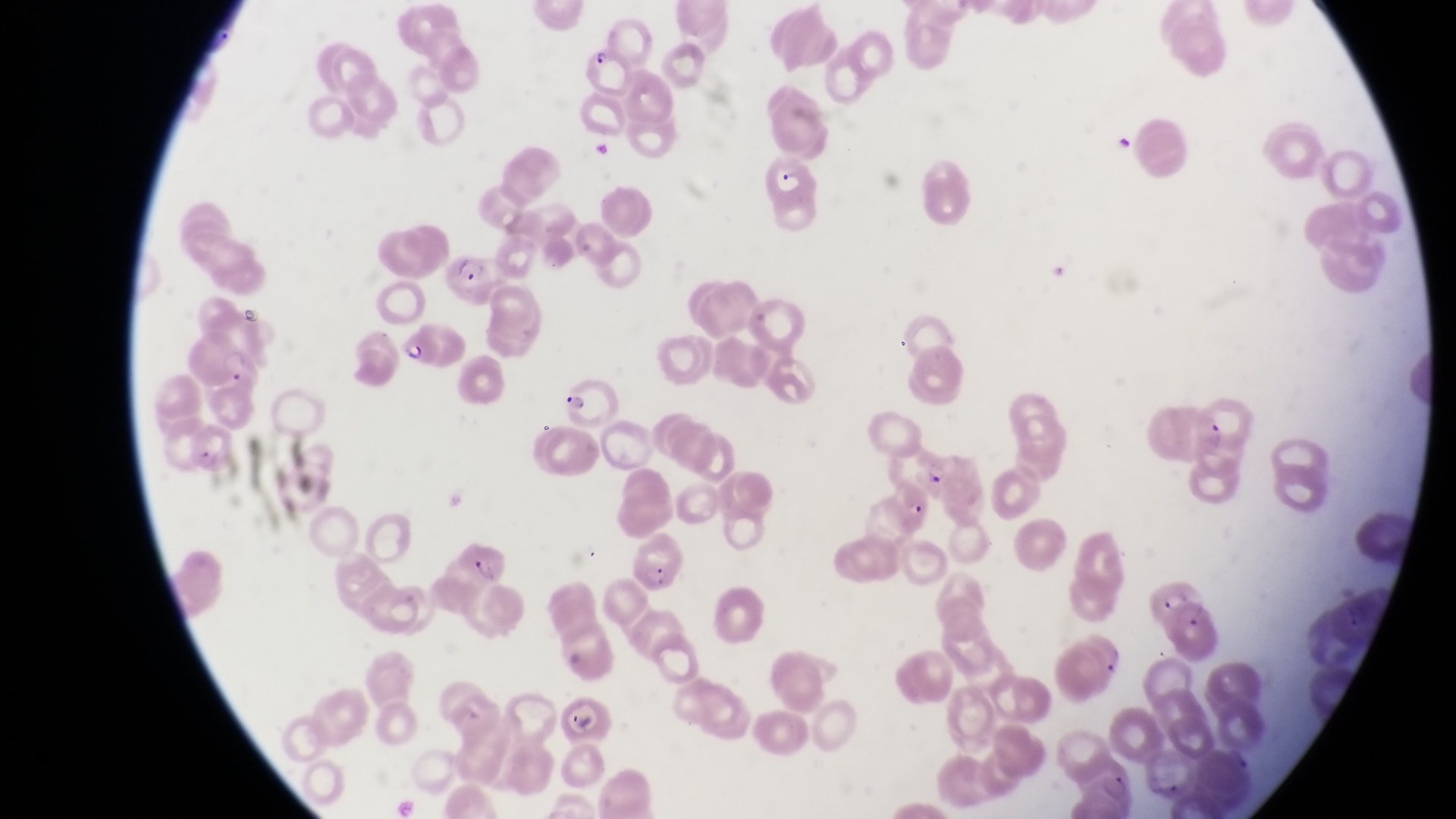
Approximate bounding boxes as {left, top, right, bottom} in pixels.
Summary:
  - Artifact (platelet-like body, stain precipitate, or debris) locations: {1115, 132, 1142, 161}
  - Parasitised red blood cell locations: {582, 42, 629, 97}, {767, 158, 819, 225}, {444, 257, 502, 303}, {397, 328, 444, 370}, {190, 331, 253, 390}, {563, 375, 615, 424}, {192, 410, 244, 479}, {920, 457, 949, 489}, {450, 539, 513, 588}, {1150, 578, 1221, 657}, {558, 701, 617, 747}
  - Image size: 1456×819 pixels
  - Country: Uganda
  - Capture: smartphone photograph through the eyepiece of an Olympus CX-23 microscope
  - Preparation: thin blood film
  - Magnification: 1000x
  - Field of view: single